Find the red blood cells that are infected with P. falciparum, and any of indeterminate infection status.
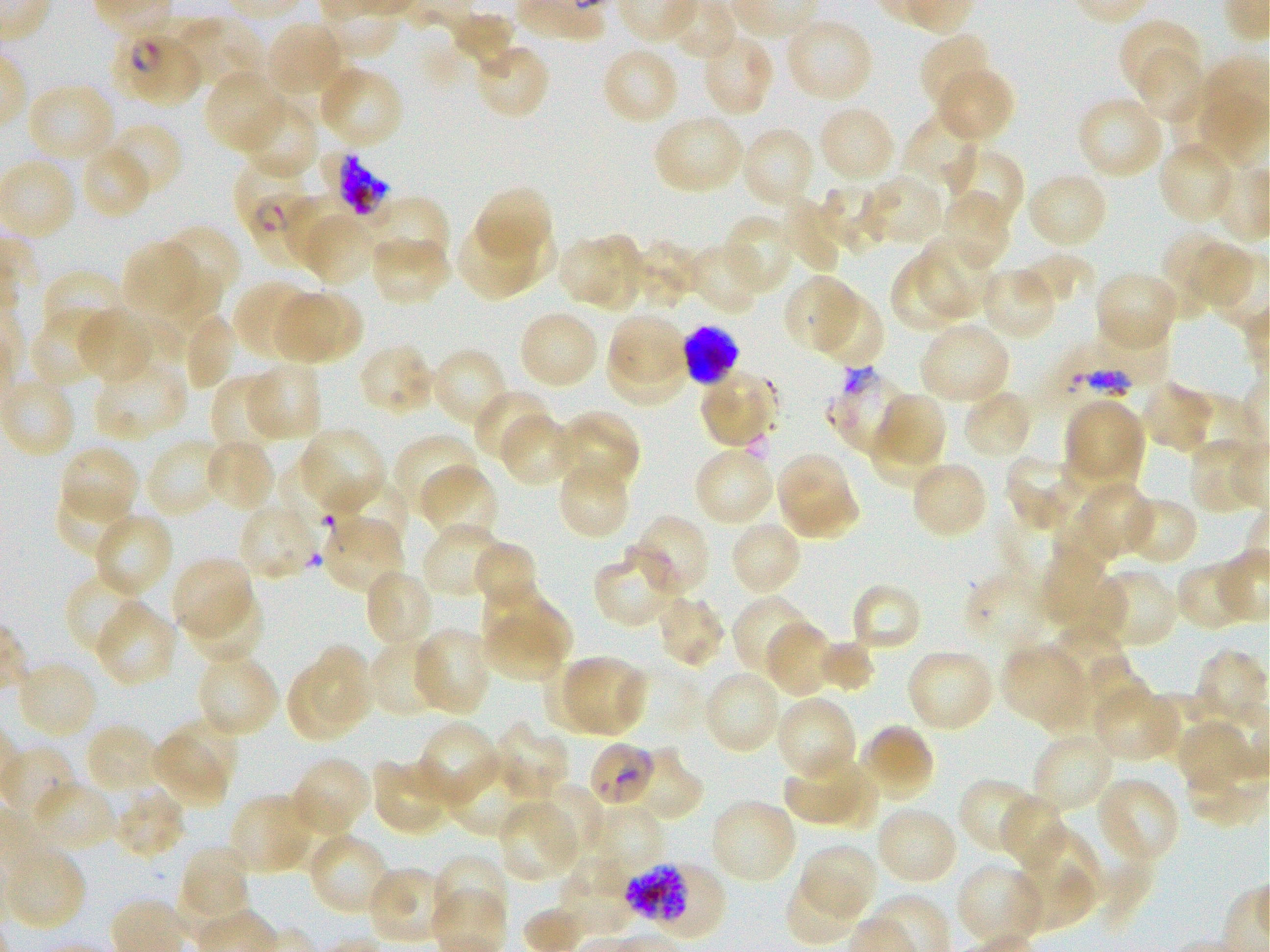
Approximate bounding rectangles given as corner coordinates in pixels from the top-left. Not every red blood cell is marked. A life-cycle stage — or a range of stages, where the recorded stages span more than one — follows each staged infected red blood cell.
Infected red blood cells: (x1=125, y1=37, x2=205, y2=107) late ring to early trophozoite; (x1=233, y1=155, x2=324, y2=262) ring; (x1=684, y1=324, x2=738, y2=385) late schizont; (x1=588, y1=740, x2=657, y2=808); (x1=629, y1=863, x2=724, y2=944) schizont.
Red blood cells of indeterminate infection status: (x1=310, y1=149, x2=406, y2=229), (x1=827, y1=364, x2=908, y2=456).

Summary:
  - Locations of uninfected red blood cells: (x1=451, y1=13, x2=518, y2=71), (x1=176, y1=15, x2=265, y2=90), (x1=782, y1=16, x2=875, y2=104), (x1=1118, y1=18, x2=1203, y2=98), (x1=264, y1=21, x2=346, y2=99), (x1=700, y1=32, x2=776, y2=119), (x1=918, y1=33, x2=992, y2=113), (x1=472, y1=42, x2=552, y2=121), (x1=600, y1=46, x2=680, y2=126), (x1=1137, y1=51, x2=1208, y2=120), (x1=316, y1=64, x2=405, y2=150), (x1=934, y1=67, x2=1015, y2=144), (x1=203, y1=70, x2=287, y2=155), (x1=33, y1=81, x2=117, y2=153), (x1=1076, y1=95, x2=1167, y2=181), (x1=238, y1=97, x2=320, y2=182), (x1=816, y1=104, x2=898, y2=185), (x1=903, y1=109, x2=983, y2=192), (x1=652, y1=114, x2=746, y2=196), (x1=113, y1=125, x2=182, y2=193), (x1=740, y1=126, x2=817, y2=211), (x1=1157, y1=140, x2=1238, y2=226), (x1=85, y1=145, x2=152, y2=216), (x1=942, y1=146, x2=1023, y2=232), (x1=1025, y1=170, x2=1110, y2=251), (x1=857, y1=172, x2=948, y2=247), (x1=824, y1=181, x2=889, y2=249), (x1=471, y1=185, x2=553, y2=268), (x1=940, y1=190, x2=1012, y2=271), (x1=281, y1=196, x2=366, y2=275), (x1=353, y1=196, x2=450, y2=282), (x1=779, y1=199, x2=844, y2=274), (x1=723, y1=214, x2=797, y2=296), (x1=454, y1=217, x2=546, y2=302), (x1=160, y1=224, x2=240, y2=310), (x1=590, y1=230, x2=644, y2=316), (x1=1159, y1=230, x2=1216, y2=320), (x1=368, y1=233, x2=451, y2=306), (x1=556, y1=234, x2=619, y2=308), (x1=914, y1=238, x2=999, y2=318), (x1=628, y1=239, x2=701, y2=309), (x1=1187, y1=240, x2=1251, y2=306), (x1=126, y1=242, x2=198, y2=316), (x1=687, y1=242, x2=766, y2=316), (x1=888, y1=253, x2=973, y2=333), (x1=1017, y1=254, x2=1087, y2=311), (x1=146, y1=264, x2=221, y2=359), (x1=38, y1=266, x2=128, y2=354), (x1=978, y1=266, x2=1058, y2=341), (x1=1093, y1=269, x2=1180, y2=354), (x1=782, y1=273, x2=863, y2=357), (x1=233, y1=280, x2=317, y2=361), (x1=814, y1=291, x2=885, y2=367), (x1=295, y1=293, x2=360, y2=357), (x1=274, y1=294, x2=337, y2=362), (x1=31, y1=304, x2=116, y2=388), (x1=74, y1=307, x2=160, y2=384), (x1=517, y1=309, x2=601, y2=391), (x1=189, y1=316, x2=233, y2=390), (x1=611, y1=316, x2=684, y2=379), (x1=919, y1=320, x2=1011, y2=406), (x1=608, y1=341, x2=690, y2=404), (x1=357, y1=343, x2=438, y2=416), (x1=429, y1=346, x2=510, y2=429), (x1=93, y1=359, x2=189, y2=442), (x1=245, y1=361, x2=322, y2=444), (x1=697, y1=368, x2=779, y2=448), (x1=210, y1=376, x2=286, y2=460), (x1=1140, y1=380, x2=1217, y2=453), (x1=473, y1=388, x2=555, y2=467), (x1=962, y1=389, x2=1034, y2=461), (x1=879, y1=392, x2=948, y2=464), (x1=1063, y1=397, x2=1145, y2=488), (x1=552, y1=409, x2=639, y2=493), (x1=498, y1=414, x2=578, y2=487), (x1=865, y1=423, x2=951, y2=493), (x1=298, y1=426, x2=387, y2=514), (x1=392, y1=433, x2=479, y2=521), (x1=204, y1=437, x2=276, y2=513), (x1=1187, y1=437, x2=1267, y2=515), (x1=144, y1=438, x2=225, y2=520), (x1=59, y1=445, x2=139, y2=525), (x1=693, y1=446, x2=777, y2=527), (x1=775, y1=451, x2=861, y2=541), (x1=1003, y1=454, x2=1082, y2=532), (x1=556, y1=456, x2=631, y2=539), (x1=280, y1=459, x2=354, y2=519), (x1=909, y1=460, x2=989, y2=540), (x1=418, y1=463, x2=499, y2=545), (x1=333, y1=471, x2=409, y2=542), (x1=1085, y1=481, x2=1158, y2=556), (x1=54, y1=484, x2=136, y2=561), (x1=1120, y1=496, x2=1199, y2=566), (x1=237, y1=501, x2=319, y2=582), (x1=1050, y1=503, x2=1113, y2=581), (x1=93, y1=512, x2=174, y2=599), (x1=631, y1=514, x2=710, y2=598), (x1=320, y1=515, x2=404, y2=595), (x1=733, y1=521, x2=800, y2=594), (x1=421, y1=523, x2=506, y2=599), (x1=403, y1=541, x2=478, y2=618), (x1=477, y1=542, x2=534, y2=601), (x1=593, y1=548, x2=681, y2=630), (x1=171, y1=555, x2=255, y2=642), (x1=1041, y1=558, x2=1129, y2=640), (x1=1174, y1=559, x2=1257, y2=630), (x1=363, y1=568, x2=435, y2=649), (x1=964, y1=569, x2=1056, y2=655), (x1=1103, y1=571, x2=1180, y2=646), (x1=69, y1=574, x2=146, y2=657), (x1=850, y1=582, x2=923, y2=653), (x1=483, y1=590, x2=572, y2=652), (x1=183, y1=591, x2=266, y2=665), (x1=654, y1=592, x2=727, y2=669), (x1=733, y1=595, x2=814, y2=682), (x1=95, y1=600, x2=177, y2=689), (x1=485, y1=619, x2=564, y2=681), (x1=765, y1=621, x2=836, y2=696), (x1=412, y1=627, x2=493, y2=717), (x1=1050, y1=632, x2=1135, y2=727), (x1=367, y1=636, x2=444, y2=719), (x1=1001, y1=642, x2=1085, y2=722), (x1=814, y1=643, x2=875, y2=690), (x1=311, y1=644, x2=373, y2=723), (x1=906, y1=647, x2=996, y2=734), (x1=1197, y1=649, x2=1269, y2=718), (x1=195, y1=650, x2=280, y2=738), (x1=564, y1=653, x2=644, y2=736), (x1=1084, y1=655, x2=1153, y2=728), (x1=16, y1=658, x2=98, y2=740), (x1=541, y1=662, x2=611, y2=735), (x1=285, y1=666, x2=359, y2=744), (x1=702, y1=669, x2=784, y2=756), (x1=1094, y1=685, x2=1181, y2=762), (x1=775, y1=694, x2=858, y2=784), (x1=1149, y1=694, x2=1222, y2=763), (x1=172, y1=718, x2=239, y2=786), (x1=414, y1=719, x2=501, y2=808), (x1=491, y1=720, x2=570, y2=802), (x1=83, y1=722, x2=163, y2=795), (x1=1182, y1=722, x2=1255, y2=790), (x1=861, y1=723, x2=936, y2=802), (x1=1031, y1=731, x2=1116, y2=814), (x1=151, y1=734, x2=231, y2=806), (x1=635, y1=746, x2=707, y2=824), (x1=784, y1=753, x2=859, y2=821), (x1=289, y1=756, x2=372, y2=839), (x1=445, y1=756, x2=536, y2=838), (x1=370, y1=758, x2=456, y2=838), (x1=825, y1=761, x2=881, y2=829), (x1=1099, y1=775, x2=1180, y2=858), (x1=956, y1=778, x2=1039, y2=857), (x1=29, y1=780, x2=119, y2=854), (x1=531, y1=782, x2=606, y2=863), (x1=112, y1=785, x2=187, y2=860), (x1=229, y1=792, x2=317, y2=873), (x1=275, y1=792, x2=351, y2=874), (x1=996, y1=794, x2=1068, y2=872), (x1=707, y1=798, x2=799, y2=885), (x1=497, y1=799, x2=582, y2=882), (x1=874, y1=804, x2=959, y2=886), (x1=586, y1=805, x2=664, y2=872), (x1=1026, y1=831, x2=1099, y2=903), (x1=312, y1=838, x2=385, y2=911), (x1=798, y1=843, x2=878, y2=923), (x1=3, y1=844, x2=88, y2=931), (x1=181, y1=845, x2=251, y2=913), (x1=432, y1=854, x2=507, y2=930), (x1=559, y1=857, x2=630, y2=936), (x1=955, y1=862, x2=1045, y2=949), (x1=1012, y1=864, x2=1092, y2=931), (x1=366, y1=865, x2=454, y2=946), (x1=784, y1=875, x2=862, y2=946)
  - Life-cycle stages observed: ring, schizont
  - Donor blood group: O+
  - Stain: Giemsa
  - Culture: in-vitro P. falciparum strain 3D7, static
  - Image size: 1270×952 pixels
  - Objective: 100x, oil immersion, numerical aperture 1.25
  - Field of view: one from this slide
  - Preparation: thin blood smear